Evaluate for malaria.
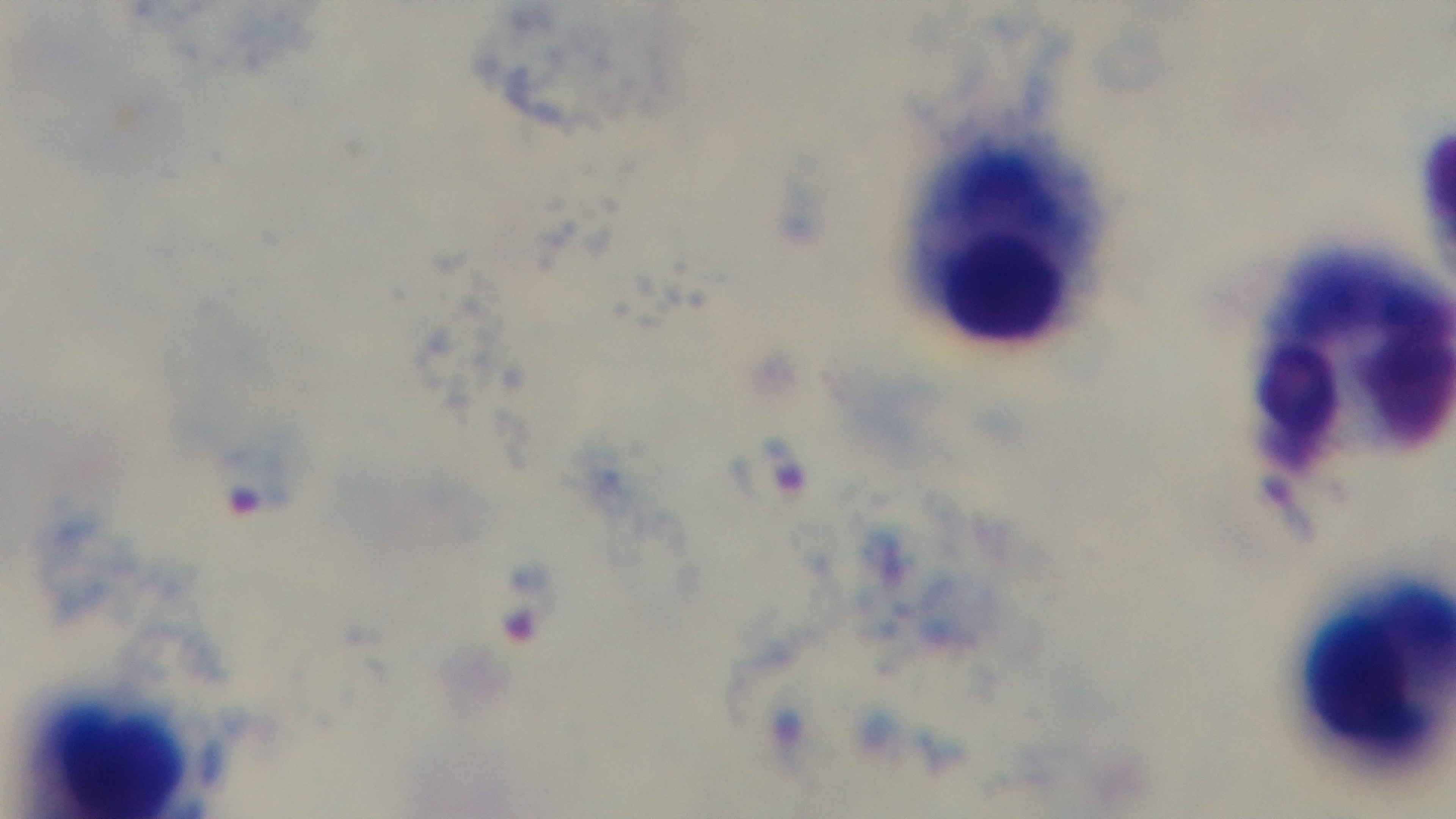

Infected.

Oil-immersion objective, 100x. Preparation: thick. Captured with a mounted 4K digital camera. Giemsa stain. Single field of view. Photomicrograph.